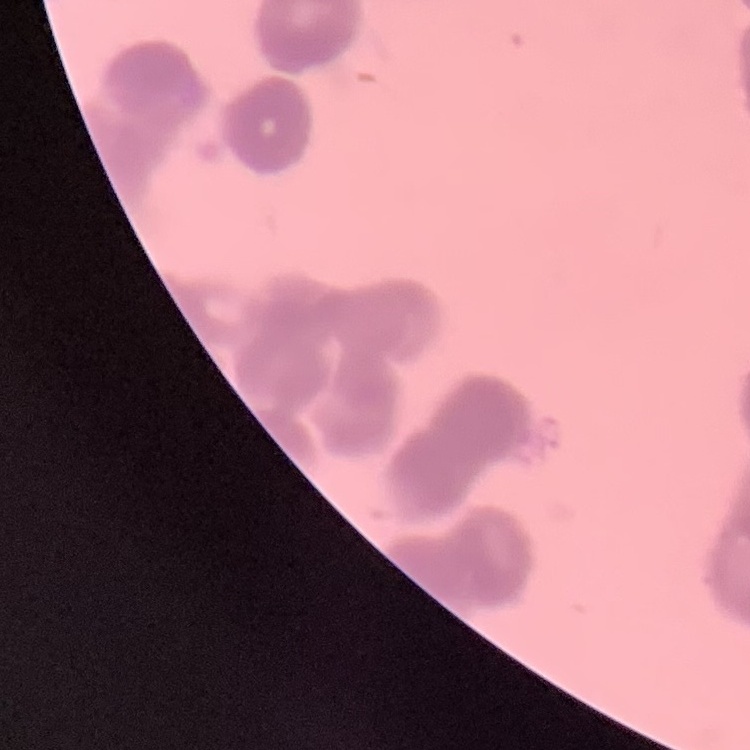

erythrocyte morphology = rouleaux formation
image type = square crop of a larger photomicrograph
stain = Field's or Giemsa
preparation = thin peripheral smear